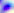
{
  "magnification": "400x",
  "modality": "photomicrograph",
  "identification": "Toxoplasma gondii"
}